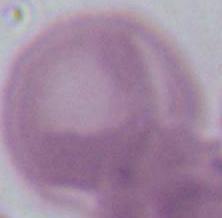

Summary:
  - Magnification: 1000x
  - Modality: photomicrograph
  - Identification: red blood cell